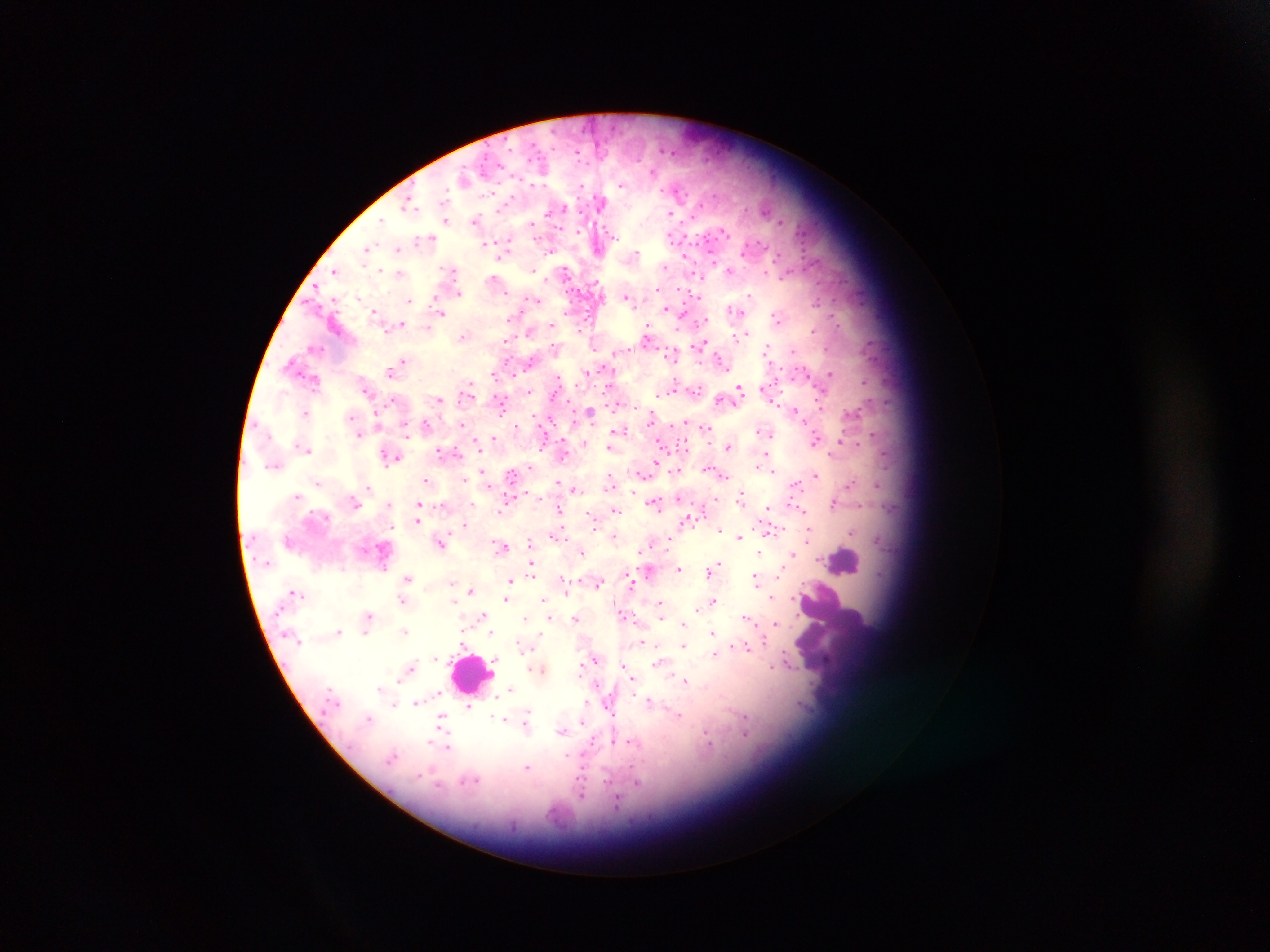
capture = mobile-phone photograph through a microscope
country = Ghana
leukocyte locations = approximate centers as (x, y) in pixels: (846, 558), (472, 670)
Plasmodium parasite locations = approximate centers as (x, y) in pixels: (540, 155), (542, 173), (464, 180), (622, 185), (406, 197), (600, 200), (566, 208), (416, 209), (671, 213), (447, 219), (475, 221), (604, 228), (725, 232), (431, 237), (670, 238), (616, 240), (367, 247), (397, 248), (683, 257), (500, 258), (714, 263), (444, 269), (450, 271), (533, 271), (765, 271), (566, 272), (335, 273), (399, 273), (783, 279), (458, 291), (690, 293), (747, 294), (630, 297), (334, 298), (408, 300), (533, 300), (667, 308), (729, 310), (376, 311), (442, 313), (773, 315), (708, 319), (779, 322), (400, 325), (510, 326), (529, 331), (648, 333), (465, 337), (736, 338), (700, 343), (767, 344), (628, 350), (403, 358), (720, 360), (675, 361), (397, 366), (801, 368), (525, 369), (390, 371), (495, 375), (829, 376), (774, 381), (738, 385), (609, 386), (671, 392), (699, 392), (553, 393), (440, 399), (822, 402), (799, 410), (590, 411), (307, 412), (552, 419), (378, 420), (684, 422), (518, 425), (465, 426), (705, 429), (621, 430), (757, 431), (359, 433), (773, 434), (872, 435), (494, 439), (840, 439), (816, 441), (864, 441), (663, 444), (727, 446), (541, 447), (608, 447), (304, 448), (666, 449), (308, 450), (440, 450), (397, 455), (765, 456), (657, 464), (708, 468), (481, 471), (774, 471), (816, 474), (608, 475), (512, 476), (643, 476), (724, 476), (426, 479), (317, 481), (851, 482), (556, 483), (796, 484), (877, 484), (368, 487), (610, 487), (575, 488), (877, 488), (297, 494), (299, 494), (716, 498), (418, 502), (737, 502), (833, 502), (657, 503), (388, 504), (864, 505), (500, 506), (767, 508), (804, 509), (559, 511), (615, 512), (591, 515), (417, 520), (688, 520), (807, 520), (465, 522), (717, 529), (810, 530), (852, 533), (553, 534), (772, 534), (613, 535), (739, 535), (441, 540), (878, 540), (530, 541), (808, 541), (501, 546), (638, 549), (582, 550), (758, 551), (792, 553), (716, 561), (678, 567), (707, 571), (532, 572), (629, 572), (407, 577), (629, 578), (757, 578), (779, 578), (450, 581), (513, 582), (599, 583), (564, 586), (508, 588), (294, 589), (567, 590), (470, 591), (299, 592), (772, 597), (542, 598), (713, 598), (504, 599), (401, 600), (453, 601), (660, 602), (622, 613), (368, 614), (626, 615), (481, 616), (575, 618), (526, 619), (549, 619), (661, 619), (748, 620), (777, 621), (683, 622), (339, 630), (406, 630), (490, 632), (711, 632), (366, 634), (537, 639), (764, 642), (461, 644), (685, 646), (738, 646), (749, 648), (716, 654), (434, 656), (789, 660), (493, 661), (773, 665), (625, 666), (492, 669), (582, 669), (409, 671), (632, 677), (400, 679), (686, 681), (511, 686), (379, 687), (648, 700), (416, 701), (394, 703), (469, 705), (803, 705), (527, 712), (370, 715), (678, 715), (504, 719), (442, 721), (581, 721), (748, 730), (561, 732), (708, 737), (430, 741), (616, 741), (630, 741), (448, 748), (394, 754), (571, 758), (529, 767), (418, 775), (475, 779), (609, 780), (639, 781), (462, 783), (582, 786), (616, 800)
image size = 1270×952 pixels
preparation = thick blood smear
field of view = single